Give the position of every malaria parasite.
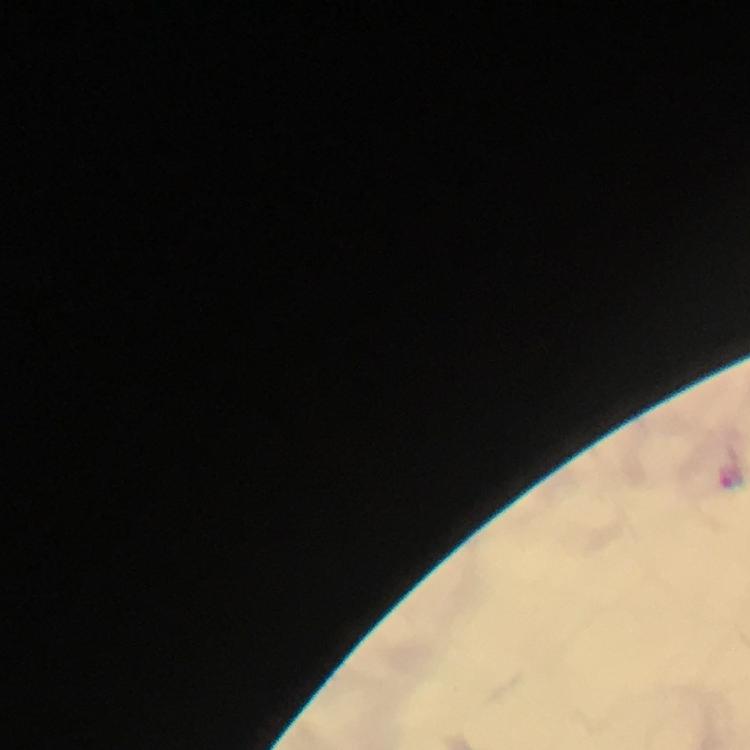
Approximate centers as [x, y] in pixels.
Malaria parasites: [731, 475].

Summary:
  - Cropped from: a single field of view
  - Magnification: 100x
  - Stain: Giemsa
  - Context: from a malaria diagnostic workup
  - Preparation: thick smear
  - Image size: 750×750 pixels
  - Capture: smartphone photograph through a microscope
  - Immersion oil: used